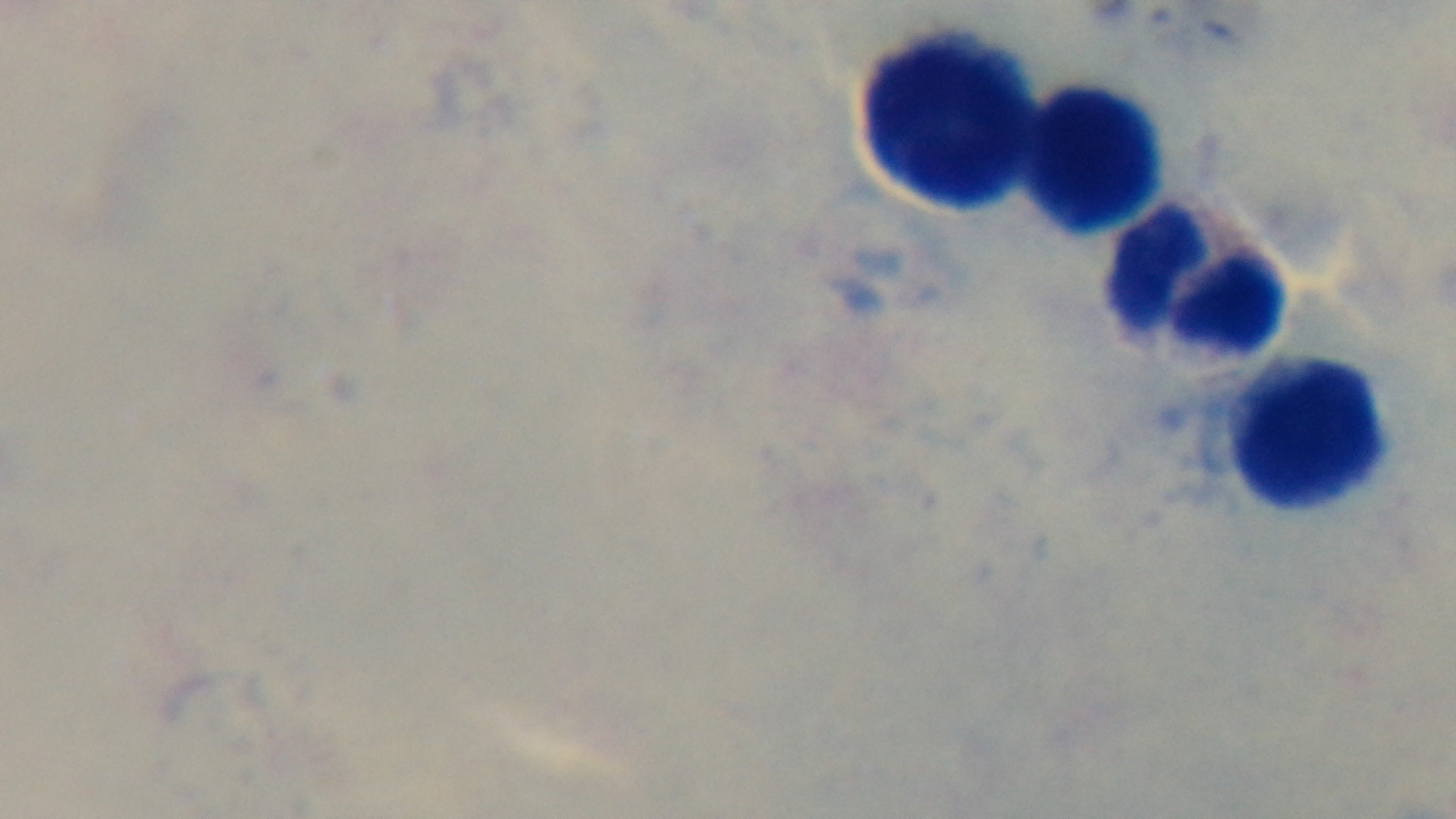

Summary:
  - Field of view: single
  - Malaria status: negative
  - Capture: mounted 4K digital camera
  - Modality: light microscopy
  - Stain: Giemsa
  - Objective: 100x oil immersion
  - Preparation: thick